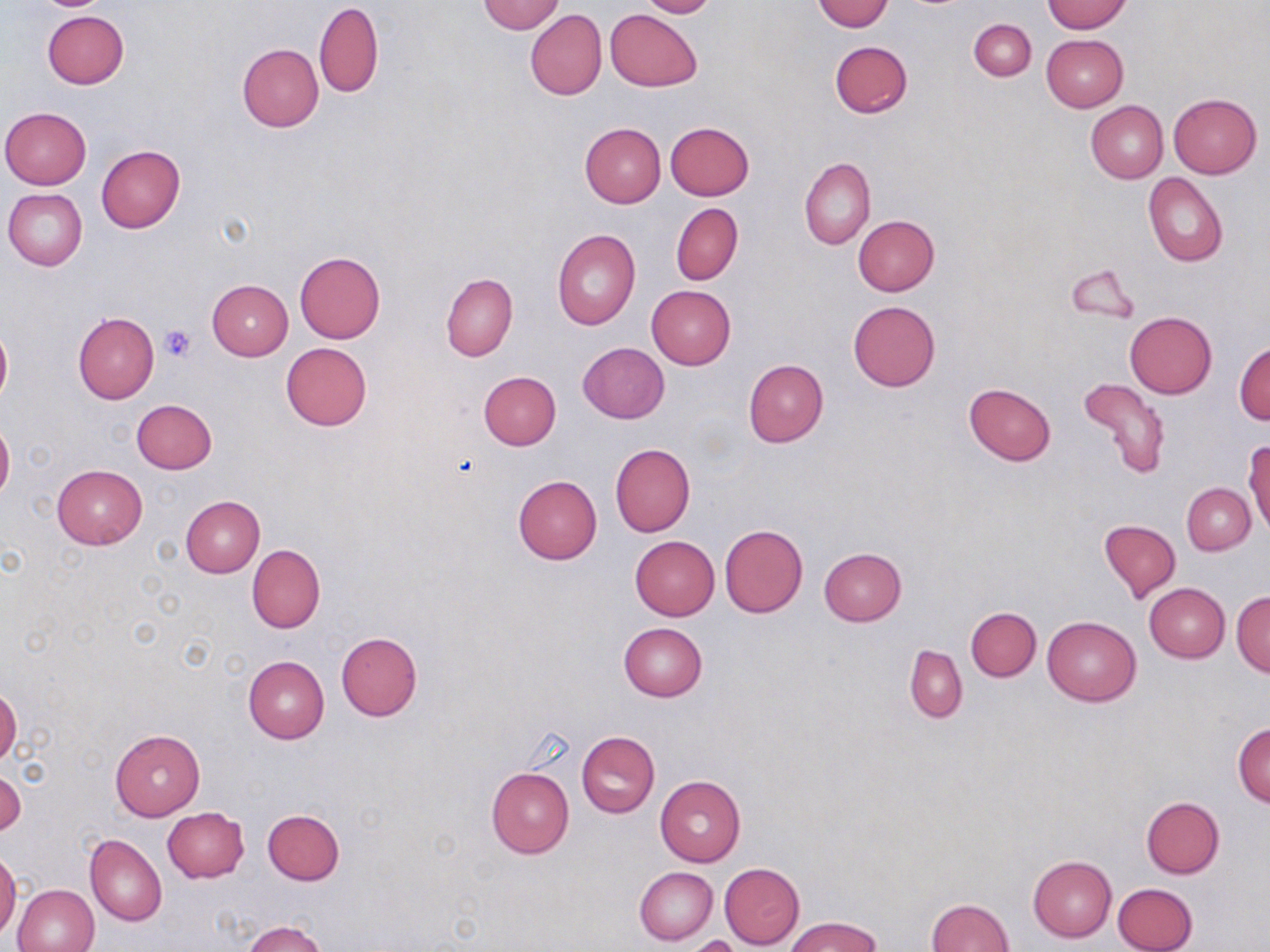 Approximate bounding boxes as (x1,y1)-(x2,y2) corner pairs in pixels. Platelet locations: (159,325)-(195,362). Uninfected red blood cell locations: (637,0)-(716,18), (813,0)-(894,32), (479,1)-(564,34), (1042,1)-(1131,34), (313,2)-(383,98), (606,9)-(701,91), (525,10)-(607,99), (42,11)-(128,89), (969,19)-(1036,80), (1041,34)-(1128,112), (829,40)-(913,118), (237,43)-(323,132), (1168,92)-(1262,178), (1086,100)-(1169,183), (1,107)-(91,189), (666,121)-(754,199), (579,122)-(666,208), (96,145)-(186,233), (799,158)-(875,250), (1143,173)-(1228,266), (3,188)-(87,271), (671,202)-(743,285), (852,215)-(939,295), (552,229)-(640,330), (294,251)-(385,344), (1066,263)-(1139,322), (441,272)-(517,361), (207,280)-(294,360), (646,285)-(736,369), (848,300)-(940,390), (1125,311)-(1217,398), (73,312)-(159,404), (0,325)-(12,404), (280,341)-(372,431), (1234,342)-(1269,425), (577,343)-(668,424), (743,359)-(827,447), (478,370)-(561,450), (1078,377)-(1171,479), (964,382)-(1057,465), (131,399)-(217,474), (0,420)-(14,501), (1245,438)-(1269,534), (610,443)-(696,536), (53,464)-(147,548), (514,475)-(602,564), (1182,483)-(1255,554), (181,496)-(265,578), (1098,519)-(1180,602), (720,524)-(808,617), (630,535)-(720,620), (247,545)-(324,632), (817,548)-(906,626), (1144,583)-(1229,662), (1232,591)-(1270,677), (965,607)-(1041,681), (1043,616)-(1141,706), (618,623)-(707,701), (335,632)-(423,721), (904,645)-(967,723), (243,655)-(329,744), (0,687)-(21,766), (1232,722)-(1269,808), (110,728)-(204,819), (576,731)-(660,817), (486,766)-(573,859), (1,769)-(24,837), (655,776)-(746,866), (1141,795)-(1225,878), (163,808)-(249,882), (263,809)-(344,885), (85,834)-(166,926), (0,851)-(20,940), (1028,855)-(1117,942), (719,863)-(805,948), (634,866)-(717,945), (1113,882)-(1198,952), (12,883)-(99,952), (925,898)-(1014,952), (785,916)-(882,952), (244,920)-(328,952), (687,935)-(743,952). Slide-level diagnosis: negative for blood parasites. May-Grünwald-Giemsa stain. Light microscopy. Thin blood film. Single field of view. Captured at 1000x magnification. Image is 1270×952 pixels.